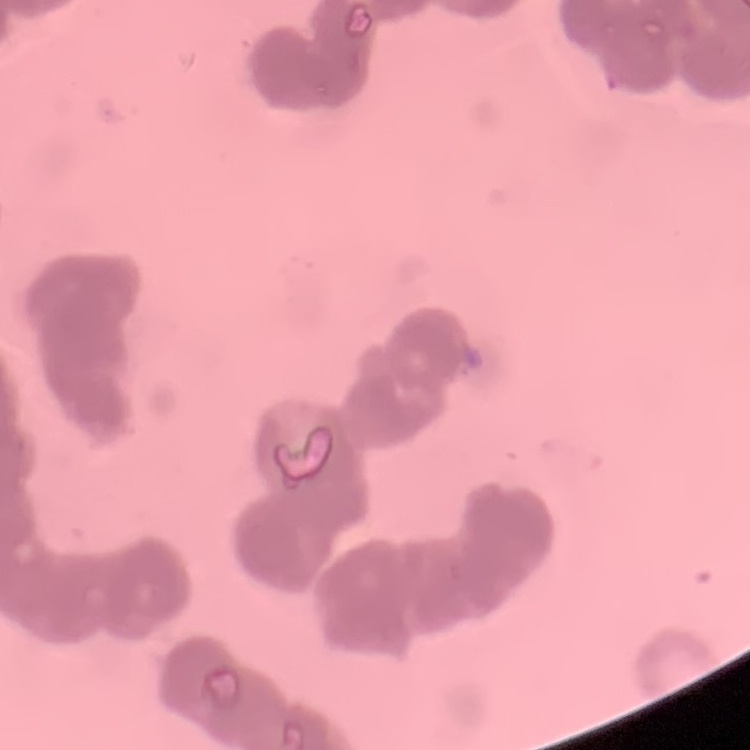
Summary:
  - Red blood cell morphology: rouleaux formation
  - Stain: Field's or Giemsa
  - Preparation: thin peripheral smear
  - Image type: one tile cut from a larger photomicrograph